Locate the cells, classifying each as a parasitized red blood cell, an uninfected red blood cell, or a white blood cell.
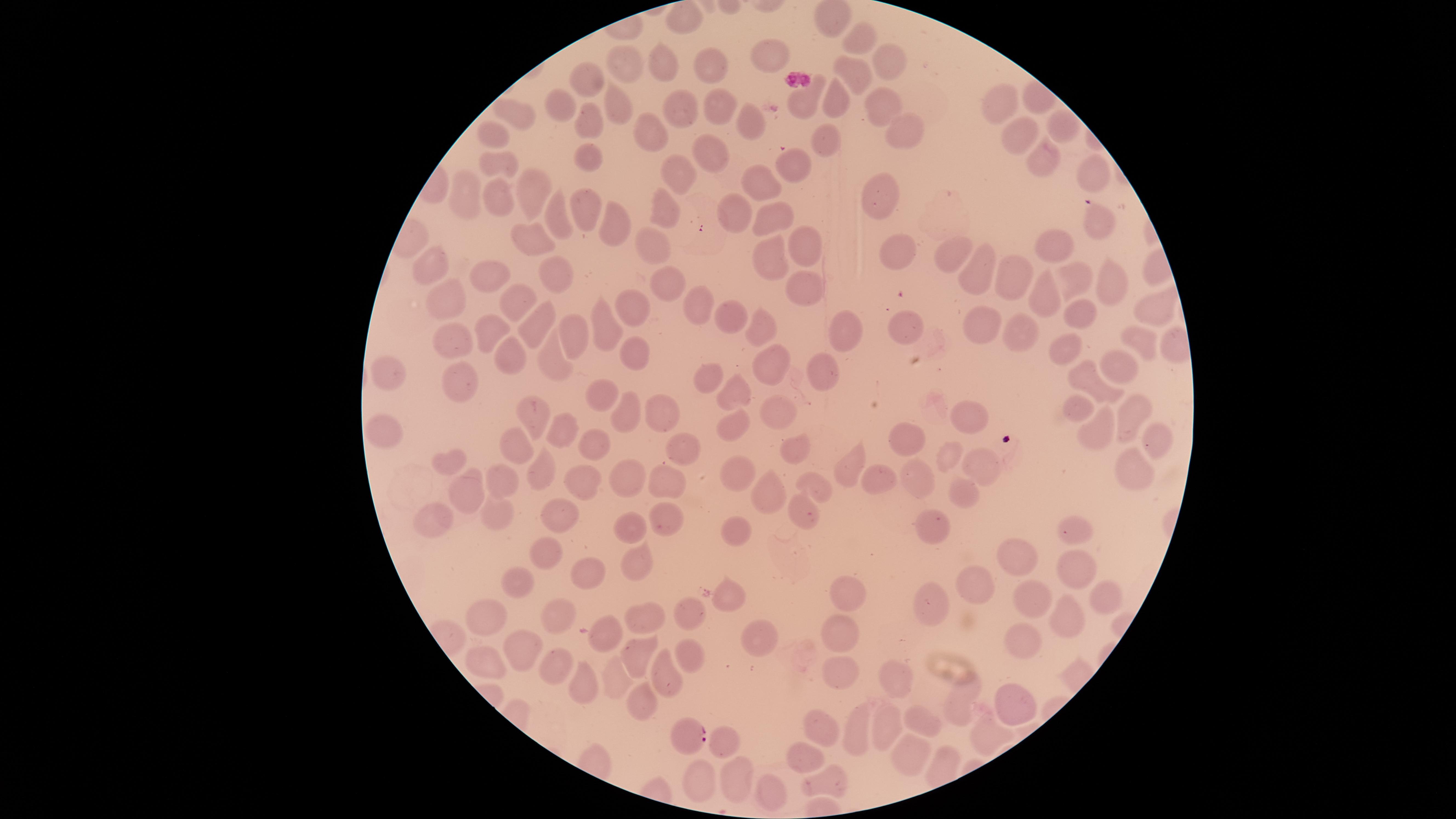

Approximate marker points as [x, y] in pixels.
Parasitized red blood cells: [686, 737].
Uninfected red blood cells: [679, 22], [864, 35], [770, 50], [623, 60], [898, 61], [714, 63], [661, 65], [850, 74], [587, 79], [834, 96], [676, 102], [715, 102], [805, 103], [1004, 103], [616, 106], [565, 107], [882, 107], [512, 120], [587, 123], [750, 126], [1061, 126], [648, 130], [1016, 132], [903, 133], [494, 138], [824, 141], [590, 152], [709, 153], [1037, 155], [792, 162], [503, 164], [680, 172], [1094, 176], [763, 182], [532, 186], [880, 192], [464, 195], [500, 197], [662, 205], [584, 208], [739, 209], [774, 213], [560, 217], [1096, 219], [617, 229], [538, 241], [652, 241], [806, 241], [1047, 241], [895, 249], [946, 255], [770, 256], [426, 267], [488, 267], [982, 273], [1108, 276], [563, 278], [1015, 279], [1080, 280], [666, 285], [804, 288], [1050, 292], [447, 297], [521, 300], [634, 303], [695, 304], [1146, 305], [1080, 309], [725, 318], [905, 321], [494, 322], [603, 322], [538, 323], [976, 323], [759, 326], [578, 327], [846, 331], [456, 333], [1021, 334], [1138, 339], [508, 346], [1066, 349], [634, 359], [551, 362], [1119, 362], [826, 365], [777, 366], [459, 369], [383, 371], [709, 377], [1100, 382], [732, 386], [599, 393], [1081, 402], [627, 409], [1135, 410], [660, 412], [776, 415], [529, 416], [973, 417], [734, 422], [562, 431], [1097, 432], [385, 434], [1156, 434], [904, 436], [598, 441], [798, 441], [686, 446], [514, 447], [946, 454], [854, 457], [451, 461], [982, 467], [1136, 468], [917, 471], [539, 472], [874, 474], [738, 475], [669, 477], [502, 479], [582, 480], [631, 480], [818, 482], [477, 484], [767, 492], [960, 494], [495, 512], [670, 512], [804, 515], [561, 523], [939, 523], [629, 525], [431, 527], [731, 527], [1076, 529], [541, 549], [1020, 562], [1075, 564], [634, 565], [591, 570], [515, 580], [984, 585], [846, 589], [1102, 592], [730, 594], [1038, 600], [930, 601], [1066, 612], [560, 614], [687, 614], [487, 617], [650, 617], [752, 627], [841, 632], [609, 633], [529, 643], [1023, 645], [639, 653], [689, 655], [486, 659], [555, 667], [667, 670], [836, 670], [897, 672], [616, 675], [581, 686], [640, 697], [1013, 701], [961, 703], [887, 715], [923, 723], [855, 724], [826, 726], [984, 734], [727, 741], [913, 747], [803, 755], [739, 778], [823, 778], [700, 785], [776, 796].
No white blood cells identified.

Summary:
  - Species: Plasmodium falciparum
  - Preparation: thin blood smear
  - Field of view: single
  - Visible region: circular
  - Image size: 1456×819 pixels
  - Stain: Giemsa
  - Capture: smartphone photograph through the microscope eyepiece